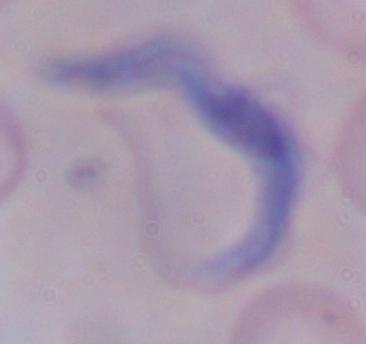 A trypanosome is shown. Micrograph. 1000x magnification.